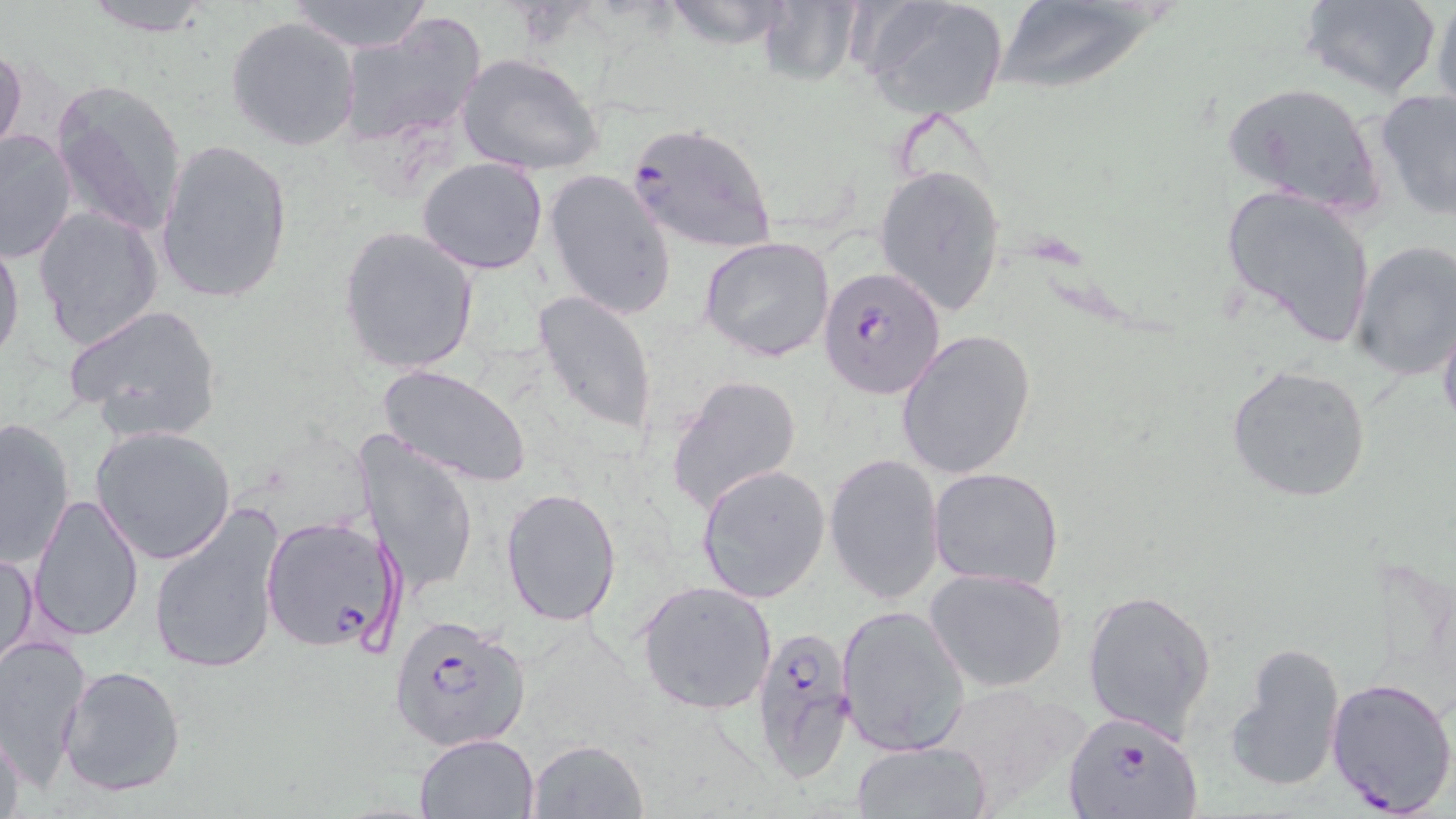
plasmodium_falciparum_infected_red_blood_cell_locations: 'approximate bounding boxes as (x1, y1, x2, y2) in pixels: (625, 123, 776, 252), (816, 265, 946, 400), (260, 514, 399, 652), (392, 614, 534, 753), (750, 621, 859, 778), (1325, 676, 1456, 814), (1061, 711, 1206, 819)'
slide_level_diagnosis: Plasmodium falciparum
preparation: thin blood smear
image_size: 1456×819 pixels
stain: May-Grünwald-Giemsa
field_of_view: one of a larger specimen
modality: optical microscopy
uninfected_red_blood_cell_locations: 'approximate bounding boxes as (x1, y1, x2, y2) in pixels: (80, 0, 216, 36), (283, 0, 432, 53), (659, 0, 801, 49), (757, 0, 864, 84), (859, 0, 1011, 120), (1297, 0, 1442, 99), (1431, 0, 1456, 122), (992, 2, 1174, 98), (338, 13, 486, 150), (225, 16, 357, 150), (0, 43, 27, 163), (456, 52, 606, 177), (50, 79, 188, 238), (1220, 81, 1389, 216), (1373, 88, 1456, 219), (0, 127, 78, 264), (154, 138, 294, 305), (417, 156, 549, 274), (873, 164, 1008, 315), (546, 169, 677, 319), (1221, 184, 1379, 346), (32, 205, 164, 351), (337, 226, 481, 376), (0, 232, 24, 370), (698, 235, 836, 363), (1349, 239, 1456, 381), (532, 291, 658, 439), (63, 303, 222, 440), (1437, 314, 1456, 435), (895, 329, 1037, 480), (1225, 363, 1372, 503), (374, 367, 532, 489), (665, 374, 801, 515), (0, 416, 76, 565), (89, 424, 237, 566), (359, 429, 479, 594), (823, 452, 945, 603), (697, 463, 831, 605), (928, 466, 1064, 591), (501, 486, 623, 627), (29, 492, 144, 641), (149, 506, 286, 676), (1, 546, 39, 675), (926, 568, 1069, 691), (636, 579, 778, 715), (1082, 588, 1217, 738), (835, 603, 972, 756), (0, 633, 91, 786), (1225, 641, 1348, 796), (58, 665, 186, 797), (924, 687, 1076, 815), (0, 723, 29, 819), (414, 731, 540, 819), (525, 738, 650, 819), (851, 741, 990, 818)'
magnification: 1000x